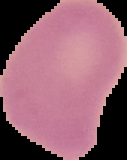

image type = cell region segmented out of the field of view; surrounding area masked to black
image size = 127×160 pixels
preparation = thin blood smear
result = negative for malaria parasites